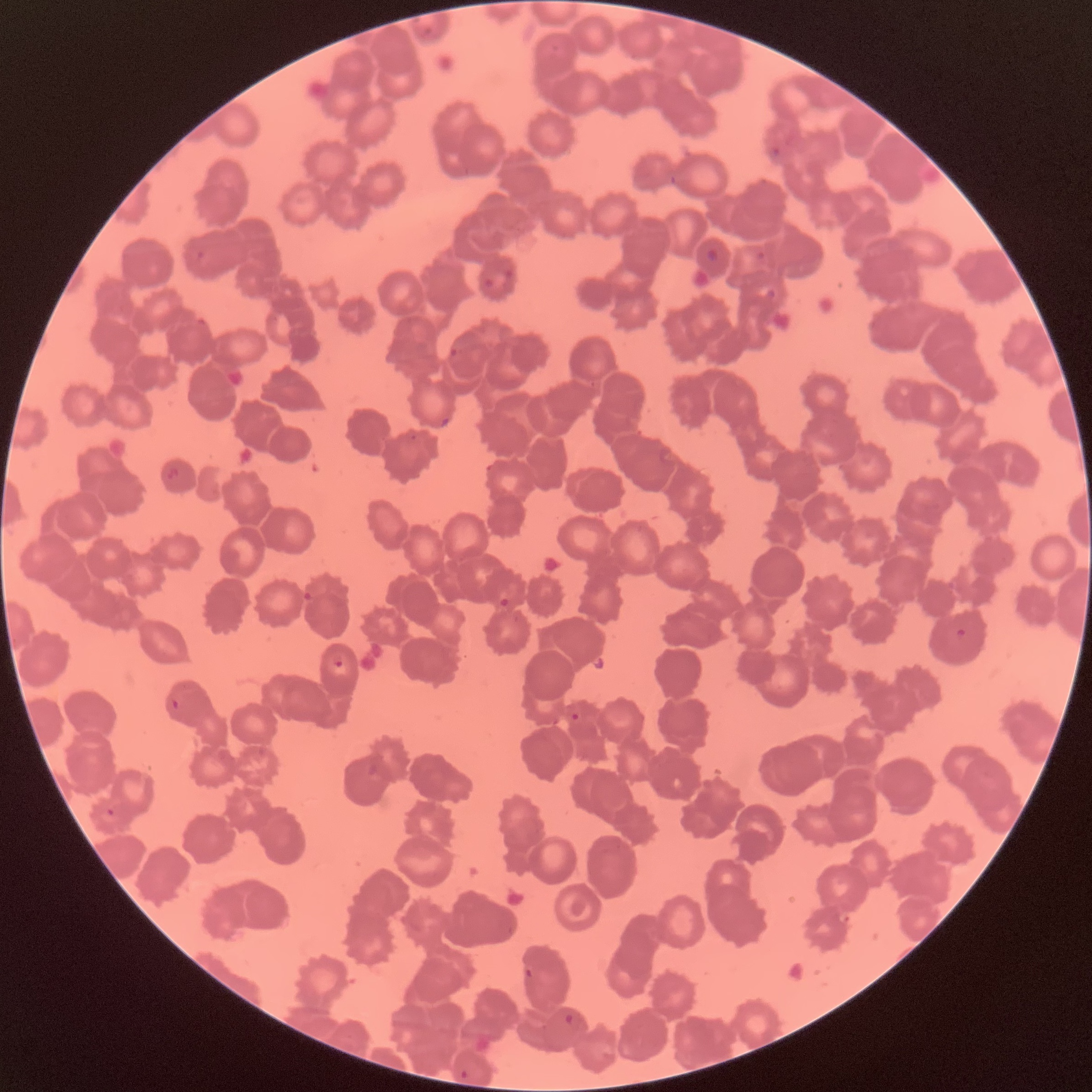

Summary:
  - Coordinate format: approximate bounding boxes as [x1, y1, x2, y2] in pixels
  - Plasmodium parasite locations: [767, 146, 781, 162], [303, 591, 313, 603], [499, 597, 510, 607], [955, 626, 969, 638], [332, 655, 344, 668], [171, 698, 180, 712], [571, 712, 580, 722], [106, 808, 115, 817], [523, 967, 534, 979], [563, 1013, 574, 1024], [460, 1068, 469, 1079]
  - Red blood cell morphology: rouleaux formation
  - Preparation: thin blood film
  - Image size: 1092×1092 pixels
  - Modality: optical microscopy